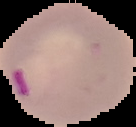 From a thin blood film. Segmented cell region on a black background. Malaria status: parasitized. Image is 136×127 pixels.